Assess this cell for malaria.
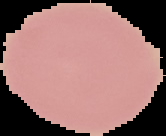

Uninfected.

image type = segmented cell region with the area outside set to black
preparation = thin blood film
image size = 166×136 pixels